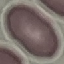 Malaria status: uninfected. Giemsa-stained preparation. Acquired by smartphone through the microscope eyepiece. Thin blood smear. Automatically extracted cell patch, resized to 64 × 64 pixels.